Outline each uninfected red blood cell.
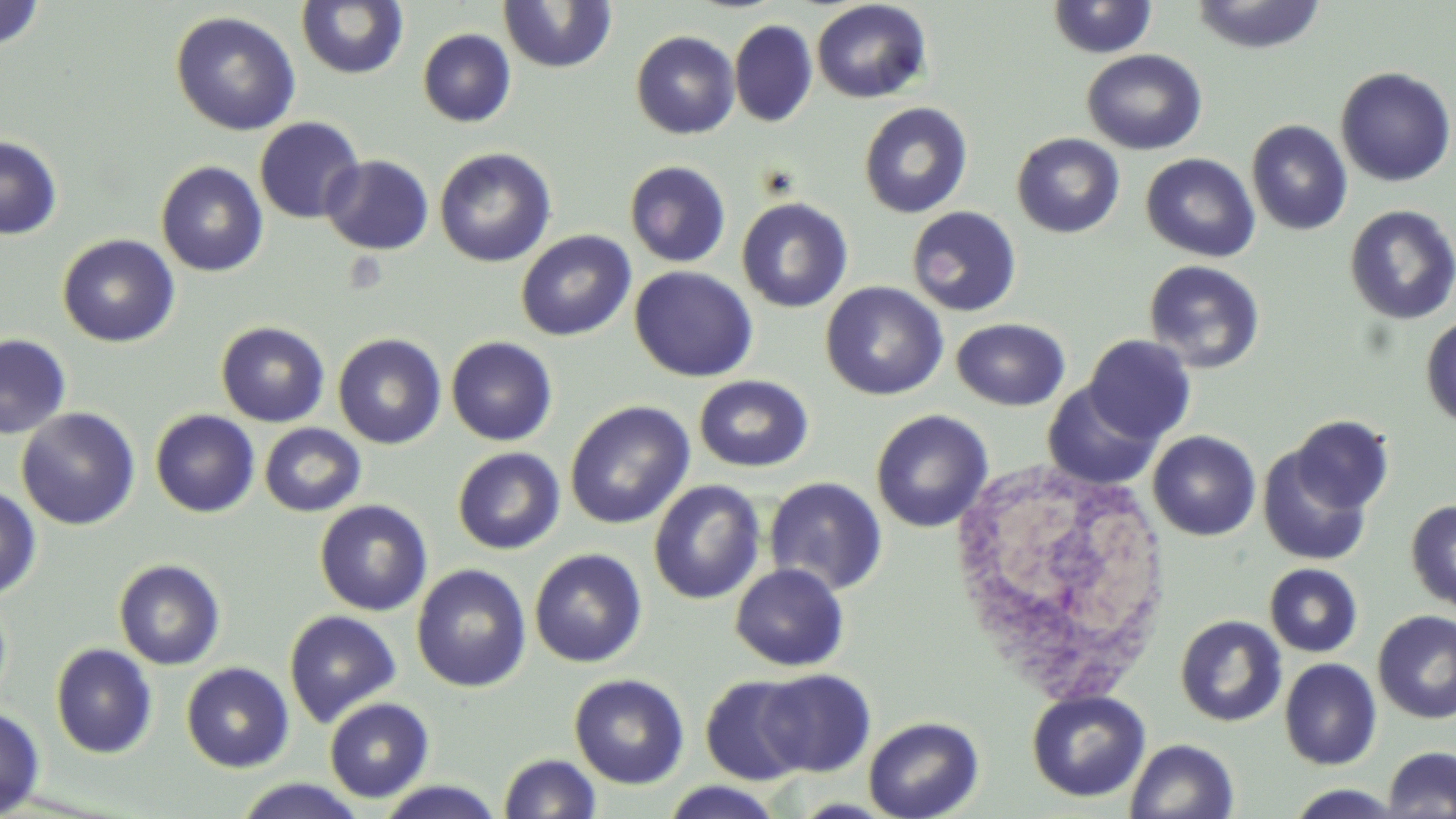

Approximate bounding boxes as named x1/y1/x2/y2 corners in pixels.
Uninfected red blood cells: (x1=497, y1=0, x2=618, y2=73), (x1=811, y1=0, x2=931, y2=103), (x1=1046, y1=0, x2=1159, y2=59), (x1=1190, y1=0, x2=1326, y2=54), (x1=0, y1=1, x2=46, y2=52), (x1=295, y1=1, x2=409, y2=80), (x1=170, y1=10, x2=301, y2=136), (x1=729, y1=19, x2=818, y2=128), (x1=417, y1=28, x2=516, y2=127), (x1=630, y1=30, x2=740, y2=139), (x1=1082, y1=49, x2=1208, y2=155), (x1=1335, y1=66, x2=1455, y2=188), (x1=857, y1=102, x2=973, y2=218), (x1=254, y1=116, x2=365, y2=224), (x1=1246, y1=119, x2=1352, y2=235), (x1=1011, y1=133, x2=1125, y2=238), (x1=0, y1=135, x2=62, y2=240), (x1=434, y1=148, x2=556, y2=268), (x1=1140, y1=152, x2=1260, y2=262), (x1=320, y1=154, x2=434, y2=255), (x1=155, y1=160, x2=269, y2=277), (x1=624, y1=160, x2=731, y2=268), (x1=736, y1=197, x2=854, y2=313), (x1=1344, y1=205, x2=1456, y2=325), (x1=905, y1=206, x2=1022, y2=317), (x1=516, y1=230, x2=636, y2=342), (x1=57, y1=233, x2=180, y2=348), (x1=1142, y1=259, x2=1266, y2=373), (x1=629, y1=266, x2=758, y2=382), (x1=820, y1=281, x2=948, y2=401), (x1=1420, y1=315, x2=1456, y2=428), (x1=951, y1=318, x2=1070, y2=411), (x1=215, y1=321, x2=330, y2=427), (x1=332, y1=333, x2=447, y2=449), (x1=0, y1=334, x2=72, y2=440), (x1=1084, y1=334, x2=1197, y2=445), (x1=446, y1=336, x2=558, y2=447), (x1=693, y1=374, x2=814, y2=473), (x1=1042, y1=381, x2=1161, y2=490), (x1=565, y1=400, x2=694, y2=529), (x1=16, y1=407, x2=141, y2=531), (x1=150, y1=409, x2=260, y2=518), (x1=870, y1=409, x2=993, y2=533), (x1=1289, y1=415, x2=1395, y2=516), (x1=259, y1=423, x2=366, y2=517), (x1=1147, y1=430, x2=1261, y2=541), (x1=1256, y1=443, x2=1375, y2=567), (x1=452, y1=447, x2=565, y2=555), (x1=763, y1=477, x2=887, y2=596), (x1=648, y1=479, x2=766, y2=605), (x1=0, y1=484, x2=41, y2=601), (x1=313, y1=499, x2=433, y2=616), (x1=1405, y1=499, x2=1456, y2=612), (x1=529, y1=548, x2=647, y2=668), (x1=112, y1=558, x2=226, y2=671), (x1=730, y1=563, x2=850, y2=671), (x1=1264, y1=563, x2=1363, y2=657), (x1=411, y1=564, x2=531, y2=692), (x1=283, y1=609, x2=402, y2=727), (x1=1372, y1=611, x2=1456, y2=724), (x1=1175, y1=615, x2=1287, y2=727), (x1=51, y1=643, x2=158, y2=759), (x1=1279, y1=658, x2=1382, y2=770), (x1=181, y1=662, x2=295, y2=772), (x1=754, y1=668, x2=875, y2=778), (x1=568, y1=674, x2=689, y2=789), (x1=700, y1=675, x2=812, y2=785), (x1=1026, y1=689, x2=1150, y2=803), (x1=324, y1=697, x2=434, y2=803), (x1=0, y1=705, x2=46, y2=816), (x1=863, y1=716, x2=983, y2=819), (x1=1124, y1=738, x2=1239, y2=818), (x1=1382, y1=746, x2=1456, y2=818), (x1=498, y1=752, x2=601, y2=818), (x1=234, y1=778, x2=367, y2=818), (x1=374, y1=779, x2=505, y2=818), (x1=659, y1=781, x2=787, y2=818), (x1=1282, y1=785, x2=1410, y2=818).

slide-level diagnosis = no evidence of blood parasites
preparation = thin blood film
field of view = single
image size = 1456×819 pixels
white blood cell locations = approximate bounding boxes as named x1/y1/x2/y2 corners in pixels: (x1=947, y1=459, x2=1174, y2=705)
modality = light microscopy
stain = May-Grünwald-Giemsa
magnification = 1000x